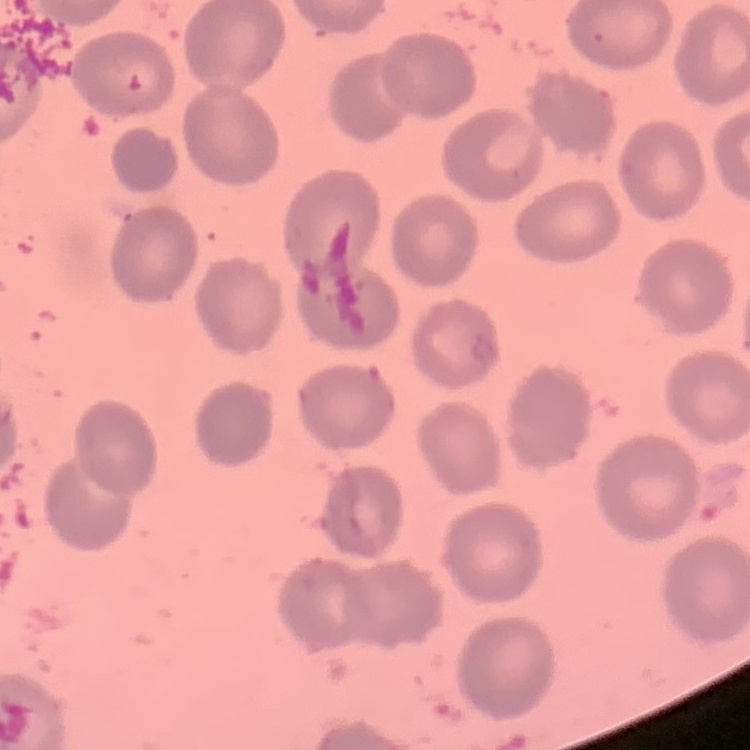

The red blood cells exhibit no rouleaux formation. Field's or Giemsa stain. Thin peripheral smear. One tile cut from a larger photomicrograph.